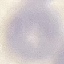
result = no malaria parasites seen
image type = cell patch, automatically extracted from a larger field of view and resized to 64 × 64 pixels
capture = smartphone camera at the microscope eyepiece
stain = Giemsa
preparation = thin blood film